Identify the parasite.
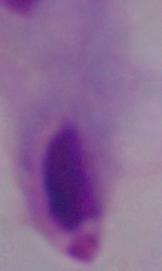
A trichomonad.

Summary:
  - Modality: photomicrograph
  - Magnification: 1000x